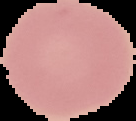
Summary:
  - Image type: segmented cell region on a black background
  - Image size: 136×121 pixels
  - Preparation: thin blood smear
  - Result: no malaria parasites detected